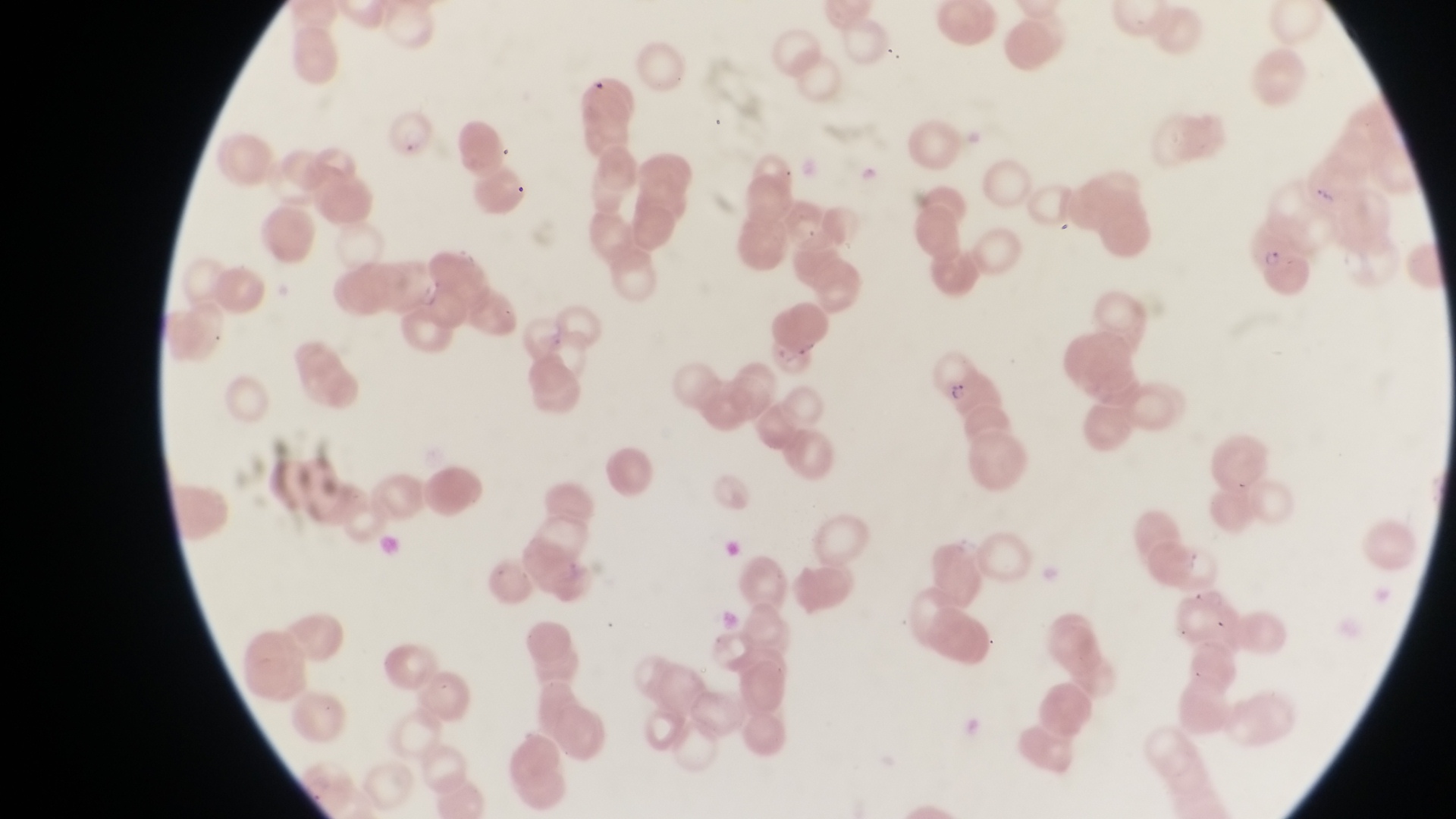

{
  "preparation": "thin blood smear",
  "country": "Uganda",
  "image_size": "1456×819 pixels",
  "parasitised_red_blood_cell_locations": "approximate bounding boxes as (left, top, right, bottom) in pixels: (384, 115, 436, 158), (1252, 222, 1311, 283), (934, 349, 984, 405)",
  "capture": "smartphone photograph through the eyepiece of an Olympus CX-23 microscope",
  "magnification": "1000x",
  "field_of_view": "single"
}